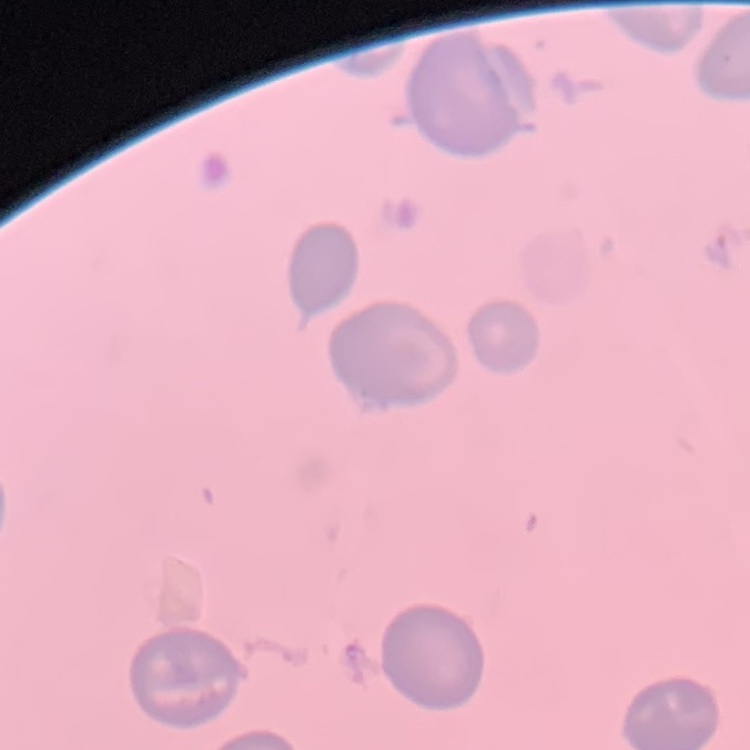

{
  "red_blood_cell_morphology": "no rouleaux formation",
  "image_type": "square crop of a larger photomicrograph",
  "preparation": "thin blood film",
  "stain": "Field's or Giemsa"
}